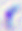 Toxoplasma gondii is seen. Captured at 400x magnification. Photomicrograph.